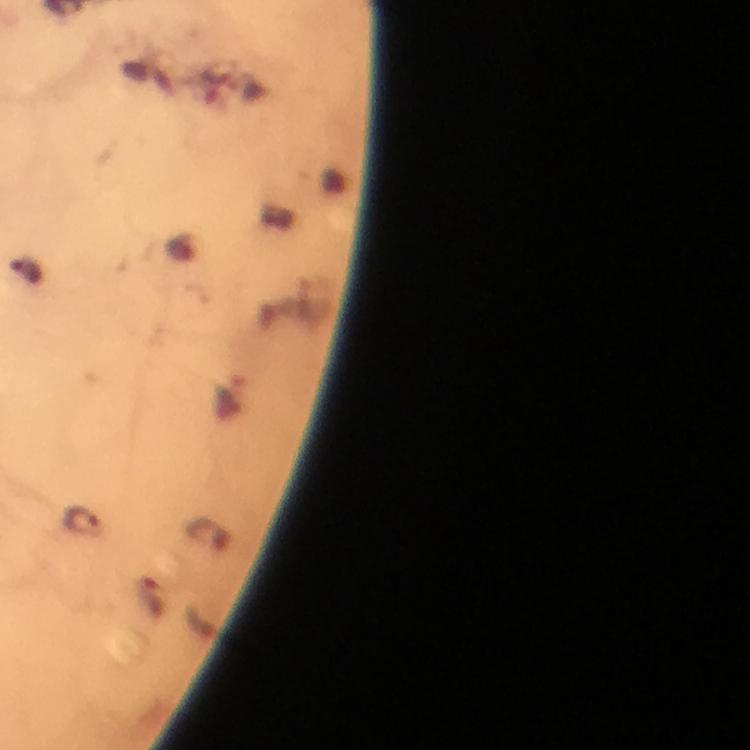
Approximate centers as (x, y) in pixels.
Summary:
  - Plasmodium parasite locations: (26, 273), (82, 520)
  - Context: from a diagnostic examination for malaria
  - Preparation: thick blood film
  - Stain: Giemsa
  - Cropped from: a single field of view
  - Magnification: 100x
  - Image size: 750×750 pixels
  - Capture: smartphone mounted on the microscope
  - Immersion oil: used